Classify this cell by malaria status.
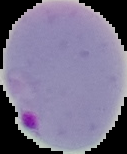

Parasitized.

image size = 127×154 pixels
image type = segmented cell region with the area outside set to black
preparation = thin blood film